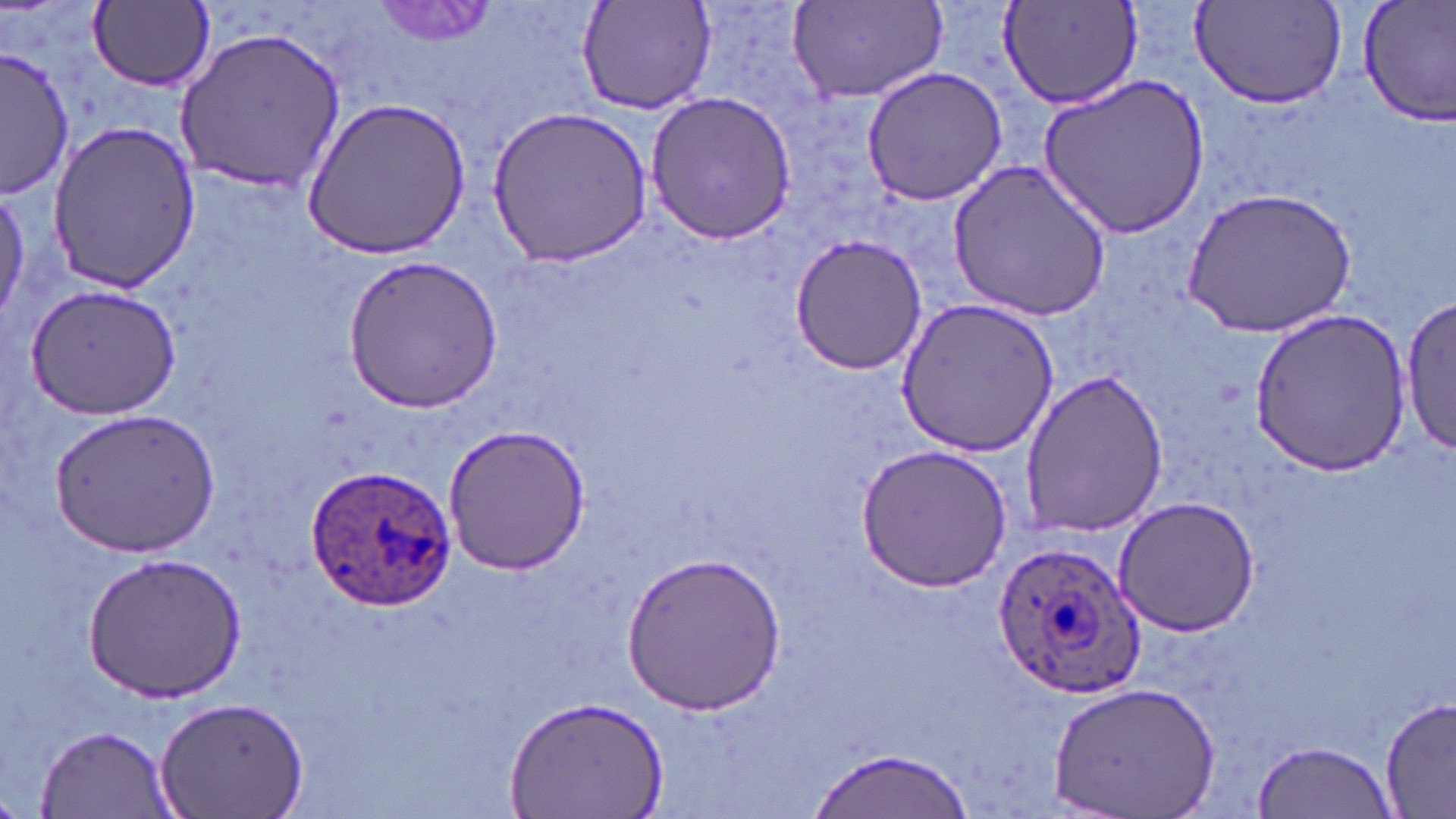

{
  "slide_level_diagnosis": "Plasmodium ovale",
  "field_of_view": "one of a larger specimen",
  "preparation": "thin blood film",
  "uninfected_red_blood_cell_locations": "approximate bounding boxes as (x1, y1, x2, y2) in pixels: (576, 0, 717, 118), (1190, 0, 1348, 114), (1356, 0, 1456, 126), (786, 2, 947, 107), (86, 3, 216, 94), (368, 3, 501, 50), (997, 3, 1143, 109), (176, 25, 346, 193), (1, 47, 76, 197), (861, 66, 1008, 206), (1037, 71, 1209, 240), (645, 91, 799, 243), (301, 98, 472, 261), (484, 105, 658, 269), (44, 118, 200, 294), (949, 160, 1112, 319), (1182, 184, 1359, 339), (788, 233, 930, 377), (341, 255, 503, 414), (23, 283, 182, 421), (1401, 296, 1455, 456), (896, 298, 1059, 457), (1250, 310, 1413, 475), (1017, 370, 1171, 536), (48, 406, 222, 560), (441, 425, 591, 575), (855, 443, 1014, 591), (1112, 495, 1260, 636), (623, 550, 786, 713), (83, 551, 247, 700), (1051, 681, 1221, 816), (501, 694, 667, 818), (1380, 694, 1455, 818), (157, 696, 309, 819), (34, 723, 174, 817), (1252, 737, 1394, 815), (807, 745, 972, 818)",
  "modality": "optical microscopy",
  "stain": "May-Grünwald-Giemsa",
  "image_size": "1456×819 pixels",
  "magnification": "1000x",
  "plasmodium_ovale_infected_red_blood_cell_locations": "approximate bounding boxes as (x1, y1, x2, y2) in pixels: (304, 463, 457, 609), (994, 540, 1145, 700)"
}